Comment on the morphology of the erythrocytes.
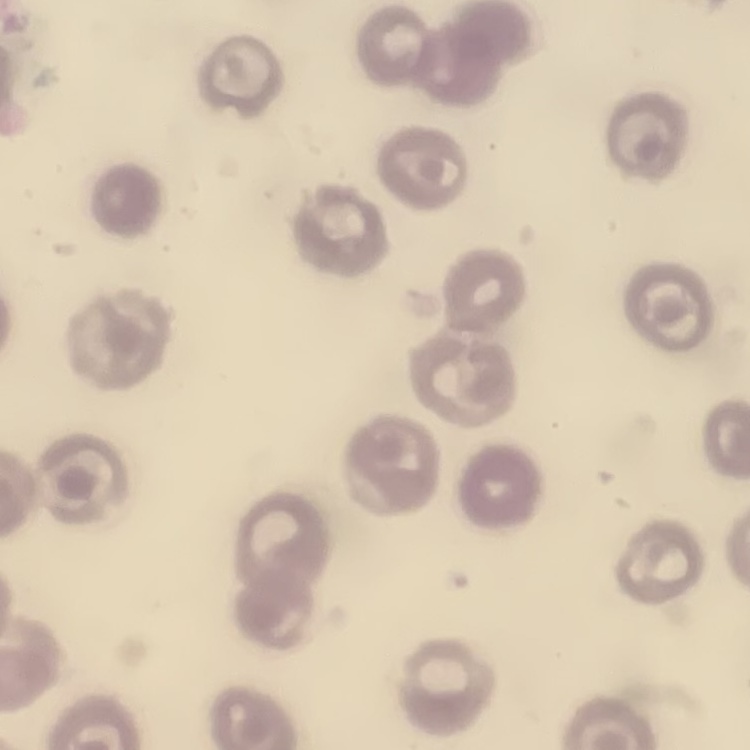

They show no rouleaux formation.

preparation = thin blood film
image type = one tile cut from a larger photomicrograph
stain = Field's or Giemsa